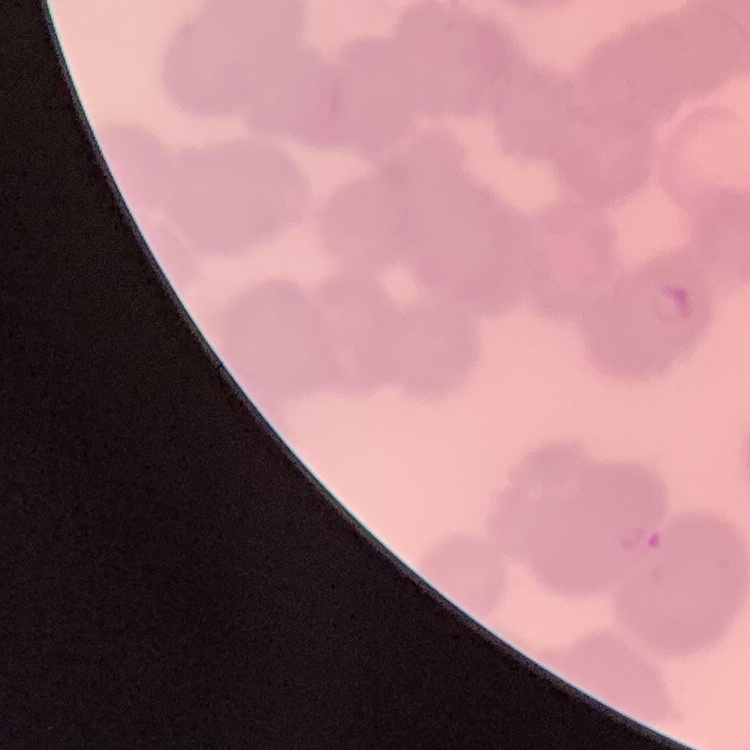
The erythrocytes show rouleaux formation. One tile cut from a larger photomicrograph. Thin blood smear. Stained with either Field's or Giemsa.